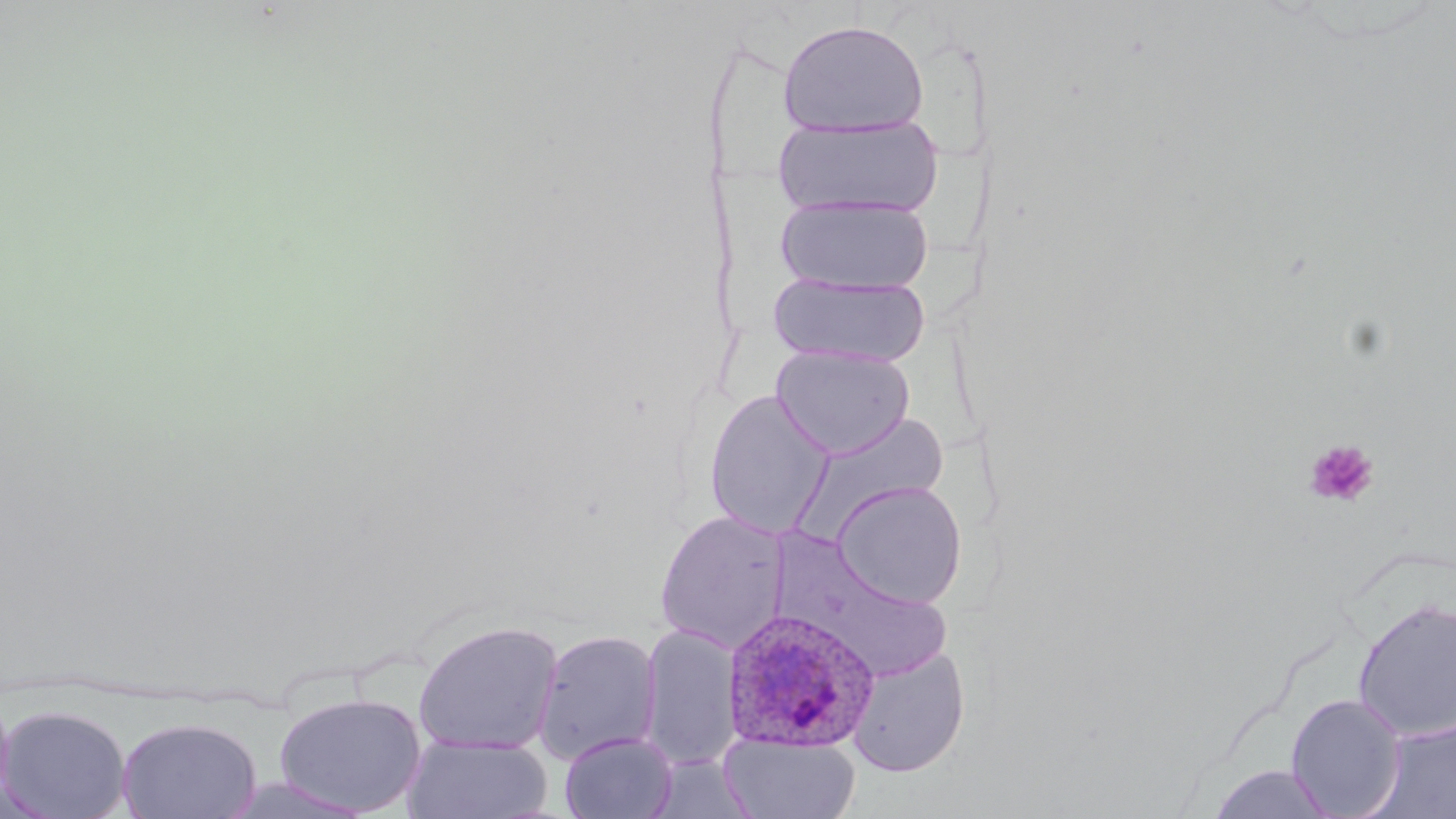

slide_level_diagnosis: Plasmodium ovale
stain: May-Grünwald-Giemsa
preparation: thin blood smear
modality: light microscopy
magnification: 1000x
plasmodium_ovale_infected_red_blood_cell_locations: 'approximate bounding boxes as (x1,y1)-(x2,y2) corner pairs in pixels: (722,607)-(879,752)'
uninfected_red_blood_cell_locations: 'approximate bounding boxes as (x1,y1)-(x2,y2) corner pairs in pixels: (777,19)-(931,138), (772,114)-(944,221), (774,194)-(935,296), (768,271)-(931,367), (770,345)-(915,459), (702,390)-(835,538), (797,414)-(952,537), (831,480)-(968,609), (654,510)-(791,653), (780,544)-(955,684), (1352,597)-(1456,742), (412,620)-(563,755), (639,623)-(742,769), (532,629)-(662,764), (846,646)-(971,776), (0,684)-(15,812), (272,691)-(428,816), (1286,694)-(1406,818), (1,703)-(133,819), (117,715)-(263,819), (1374,717)-(1456,819), (560,731)-(678,819), (720,733)-(860,818), (403,734)-(552,819), (1204,764)-(1339,819)'
field_of_view: one of a larger specimen
image_size: 1456×819 pixels
platelet_locations: 'approximate bounding boxes as (x1,y1)-(x2,y2) corner pairs in pixels: (1303,439)-(1379,508)'